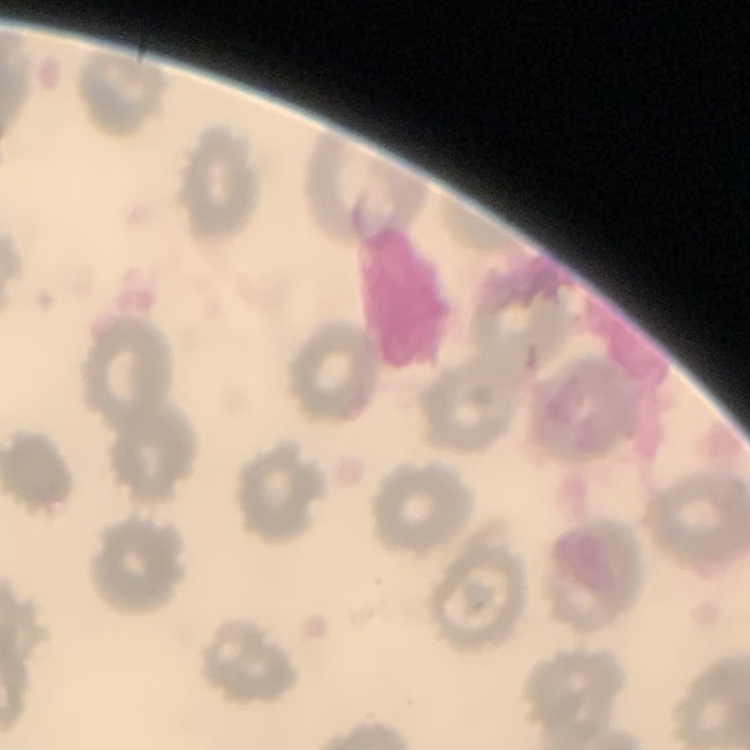 The erythrocytes exhibit no rouleaux formation. Square crop of a larger photomicrograph. Stained with either Field's or Giemsa. Thin peripheral smear.